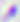

Summary:
  - Modality: photomicrograph
  - Identification: Toxoplasma gondii
  - Magnification: 400x